Comment on the morphology of the erythrocytes.
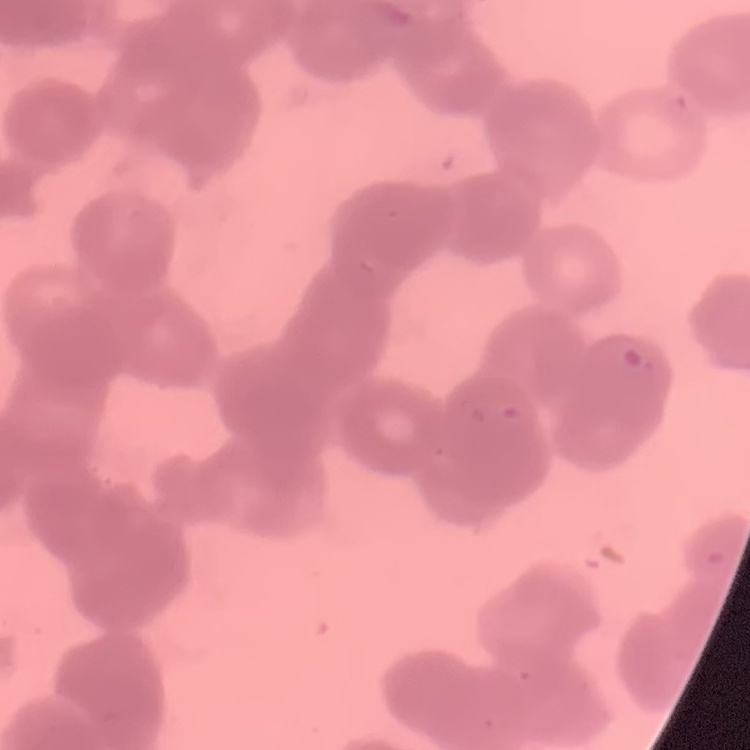
They show rouleaux formation.

Thin blood smear. Field's or Giemsa stain. Square crop of a larger photomicrograph.